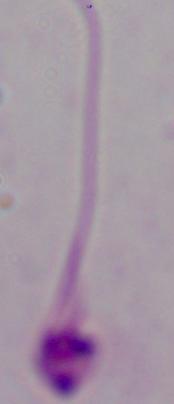

magnification = 1000x
modality = micrograph
identification = Leishmania